Outline each blood parasite and name the species.
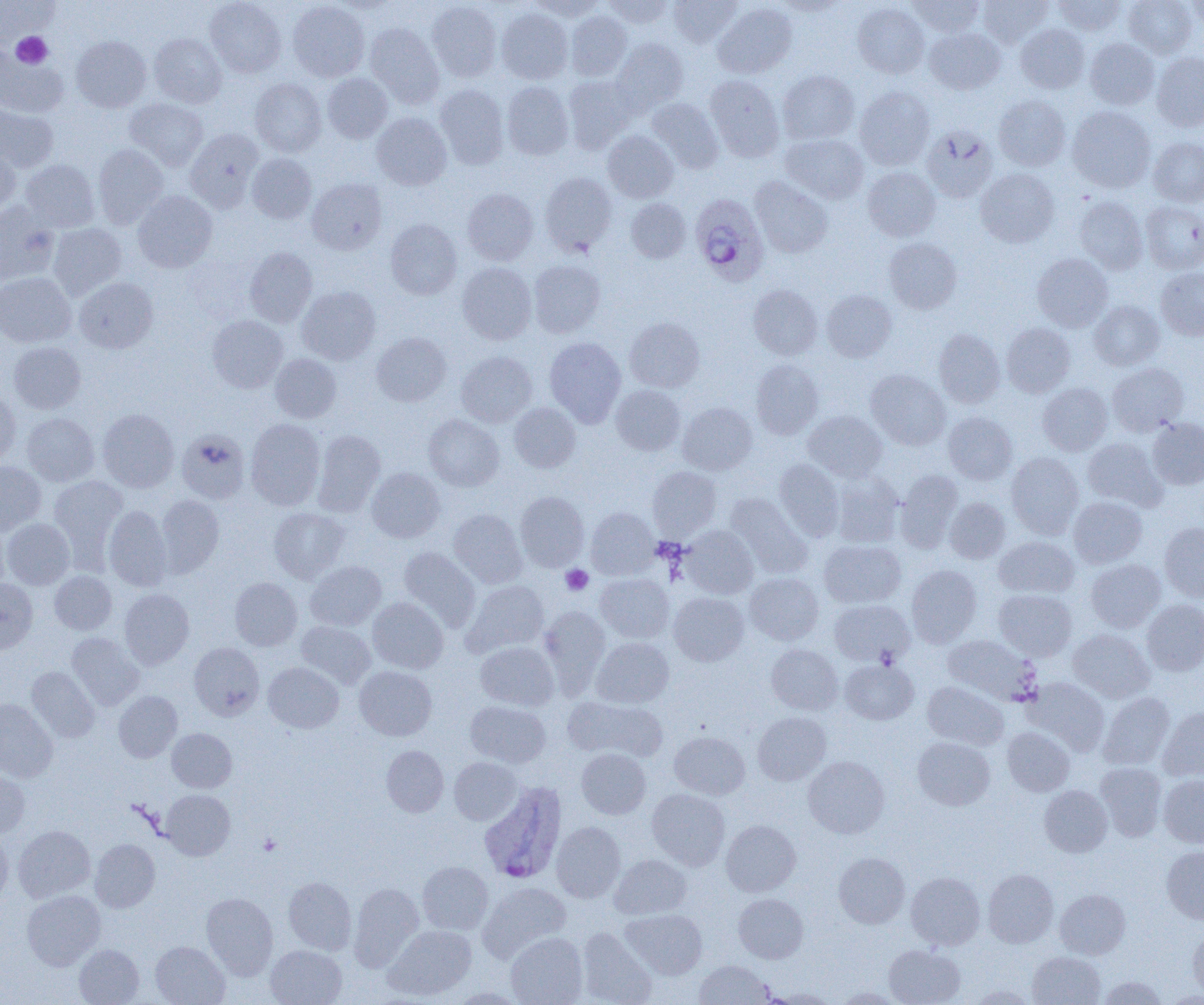

Approximate bounding boxes as (x1, y1, x2, y2) in pixels.
Plasmodium ovale-infected red blood cells: (690, 193, 769, 286), (478, 781, 568, 885).
No Plasmodium falciparum, Plasmodium malariae, Plasmodium vivax, Babesia divergens, or Trypanosoma brucei observed.

Platelet locations: (12, 32, 53, 68), (560, 565, 593, 595), (258, 833, 281, 855). Uninfected red blood cell locations: (205, 0, 286, 77), (528, 0, 606, 21), (602, 0, 674, 29), (668, 0, 742, 47), (775, 0, 848, 16), (908, 0, 985, 36), (977, 0, 1052, 48), (1053, 0, 1126, 35), (1124, 0, 1197, 59), (1185, 0, 1204, 28), (1, 1, 56, 45), (288, 1, 369, 82), (427, 1, 502, 82), (852, 2, 929, 78), (713, 3, 797, 79), (496, 7, 574, 84), (566, 11, 632, 80), (365, 23, 444, 107), (1016, 24, 1089, 93), (924, 27, 1006, 94), (150, 33, 226, 108), (71, 36, 151, 112), (612, 38, 689, 113), (1085, 38, 1159, 109), (0, 51, 68, 117), (1152, 53, 1204, 131), (777, 70, 859, 144), (323, 73, 393, 143), (563, 75, 637, 154), (704, 75, 785, 161), (250, 78, 326, 157), (502, 82, 573, 160), (435, 84, 508, 169), (855, 86, 935, 170), (994, 95, 1071, 170), (125, 98, 208, 170), (647, 98, 723, 173), (0, 102, 58, 173), (1067, 106, 1156, 192), (371, 113, 452, 190), (921, 126, 998, 203), (185, 128, 263, 212), (603, 130, 679, 202), (781, 133, 868, 204), (1148, 137, 1204, 207), (0, 144, 21, 217), (93, 144, 168, 229), (247, 153, 317, 224), (20, 159, 100, 232), (863, 167, 940, 241), (975, 168, 1059, 248), (539, 172, 617, 255), (750, 176, 832, 258), (307, 178, 386, 254), (462, 188, 538, 265), (132, 191, 217, 272), (1075, 196, 1148, 274), (626, 198, 691, 263), (1141, 201, 1204, 273), (0, 202, 59, 286), (385, 219, 462, 299), (48, 223, 127, 300), (884, 238, 962, 313), (245, 247, 317, 327), (1032, 253, 1112, 331), (528, 260, 605, 338), (457, 262, 536, 344), (1156, 268, 1204, 340), (0, 272, 76, 347), (74, 277, 158, 353), (748, 284, 822, 359), (297, 286, 380, 365), (821, 289, 896, 362), (1089, 300, 1165, 370), (207, 315, 288, 392), (625, 317, 704, 392), (1002, 322, 1075, 397), (934, 329, 1005, 407), (372, 332, 451, 406), (544, 337, 626, 426), (8, 342, 86, 414), (456, 351, 537, 427), (270, 353, 341, 423), (751, 360, 823, 439), (1107, 362, 1188, 436), (865, 369, 950, 450), (1038, 382, 1112, 456), (611, 384, 685, 455), (0, 389, 20, 466), (678, 401, 757, 475), (509, 403, 580, 473), (97, 409, 179, 492), (803, 410, 888, 482), (943, 412, 1017, 484), (22, 413, 99, 486), (424, 414, 504, 491), (1146, 417, 1204, 490), (245, 419, 325, 509), (177, 429, 250, 504), (312, 429, 385, 516), (1083, 437, 1167, 511), (1006, 452, 1083, 538), (774, 459, 845, 541), (0, 462, 46, 535), (648, 466, 721, 538), (366, 467, 445, 542), (895, 470, 963, 552), (830, 473, 904, 547), (49, 476, 128, 560), (515, 491, 589, 571), (725, 492, 812, 578), (155, 494, 223, 577), (1068, 496, 1147, 568), (944, 497, 1010, 564), (104, 505, 172, 591), (268, 507, 351, 584), (586, 507, 659, 580), (449, 509, 526, 587), (3, 518, 75, 589), (0, 519, 10, 596), (1159, 522, 1204, 602), (681, 526, 758, 598), (994, 536, 1079, 598), (819, 539, 905, 608), (398, 546, 481, 631), (1086, 559, 1166, 632), (305, 560, 386, 630), (906, 564, 981, 647), (49, 571, 116, 634), (744, 572, 823, 645), (595, 573, 674, 643), (230, 577, 302, 650), (0, 578, 38, 655), (462, 579, 549, 657), (119, 588, 194, 669), (994, 589, 1077, 661), (668, 592, 749, 666), (368, 597, 448, 674), (1141, 599, 1204, 676), (829, 600, 914, 666), (539, 606, 610, 695), (296, 621, 376, 689), (1068, 628, 1155, 702), (67, 633, 144, 710), (943, 635, 1040, 705), (591, 637, 674, 708), (475, 641, 559, 711), (189, 643, 264, 720), (766, 644, 843, 714), (840, 659, 918, 724), (263, 662, 343, 733), (27, 666, 99, 742), (354, 666, 437, 741), (1025, 677, 1110, 755), (922, 681, 1008, 749), (114, 691, 182, 762), (1098, 692, 1175, 769), (564, 697, 666, 761), (0, 698, 58, 782), (465, 700, 551, 768), (1157, 707, 1204, 781), (753, 712, 831, 785), (1003, 727, 1074, 795), (167, 728, 236, 792), (669, 731, 750, 799), (913, 736, 995, 810), (381, 745, 449, 817), (576, 748, 650, 819), (803, 756, 889, 838), (449, 757, 522, 824), (1095, 762, 1167, 841), (0, 769, 30, 838), (1158, 774, 1204, 848), (1039, 785, 1112, 856), (647, 788, 730, 870), (161, 790, 235, 859), (721, 820, 800, 896), (551, 821, 626, 903), (13, 825, 95, 902), (0, 831, 12, 908), (89, 838, 160, 912), (1161, 846, 1204, 924), (833, 852, 909, 928), (609, 854, 691, 919), (417, 861, 493, 934), (983, 869, 1058, 947), (906, 872, 985, 949), (283, 877, 356, 954), (477, 882, 571, 962), (349, 883, 423, 971), (1055, 889, 1130, 959), (22, 890, 105, 970), (201, 892, 278, 979), (733, 893, 808, 963), (621, 909, 707, 979), (384, 925, 476, 1000), (576, 927, 657, 1005), (1187, 927, 1204, 1000), (506, 932, 587, 1005), (150, 941, 230, 1005), (74, 944, 144, 1004), (265, 944, 346, 1005), (883, 944, 965, 1005), (1028, 951, 1105, 1005), (694, 960, 773, 1004), (1097, 975, 1167, 1004), (968, 985, 1037, 1004), (835, 987, 905, 1004), (764, 989, 837, 1004). Slide-level diagnosis: Plasmodium ovale. Thin blood film. Optical microscopy. One field of a larger specimen. Image is 1204×1005 pixels. Captured at 1000x magnification.